Name the parasite shown.
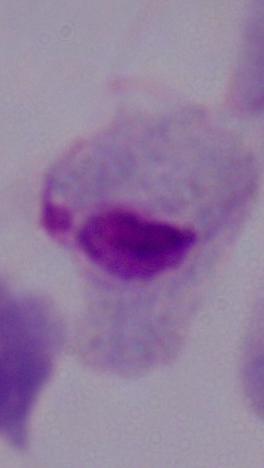

A trichomonad.

Summary:
  - Modality: micrograph
  - Magnification: 1000x